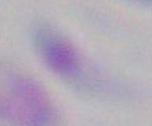
Summary:
  - Magnification: 1000x
  - Identification: Toxoplasma gondii
  - Modality: micrograph